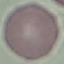

result: no malaria parasites detected
capture: smartphone camera at the microscope eyepiece
image_type: automatically extracted cell patch, resized to 64 × 64 pixels
stain: Giemsa
preparation: thin blood smear